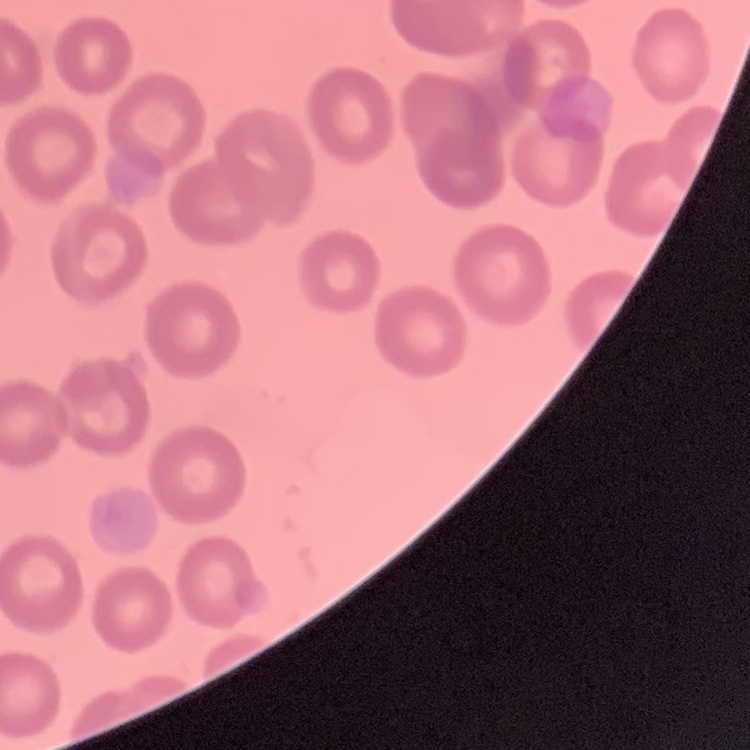
erythrocyte morphology = no rouleaux formation
preparation = thin peripheral smear
stain = Field's or Giemsa
image type = square crop of a larger photomicrograph